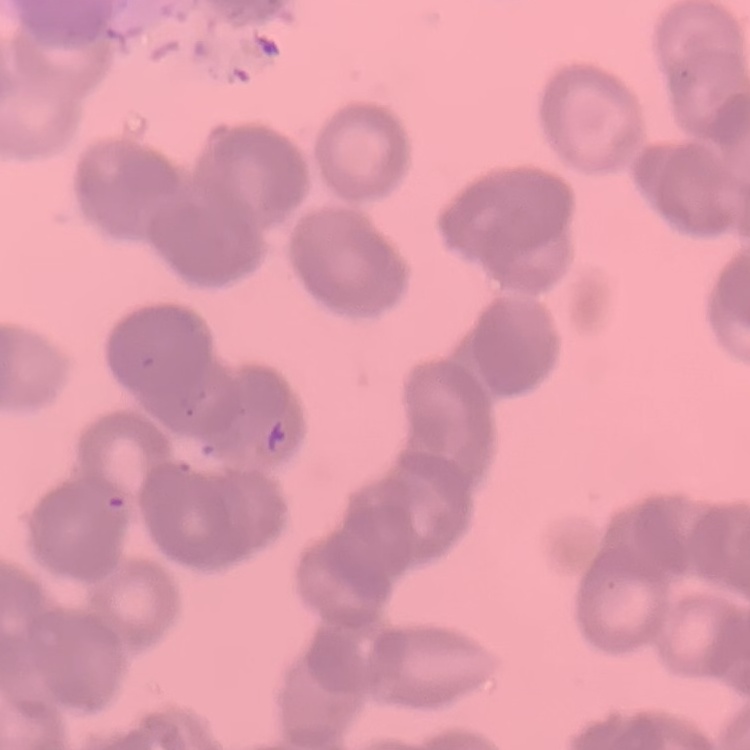

erythrocyte morphology = rouleaux formation
stain = Field's or Giemsa
image type = square crop of a larger photomicrograph
preparation = thin peripheral smear